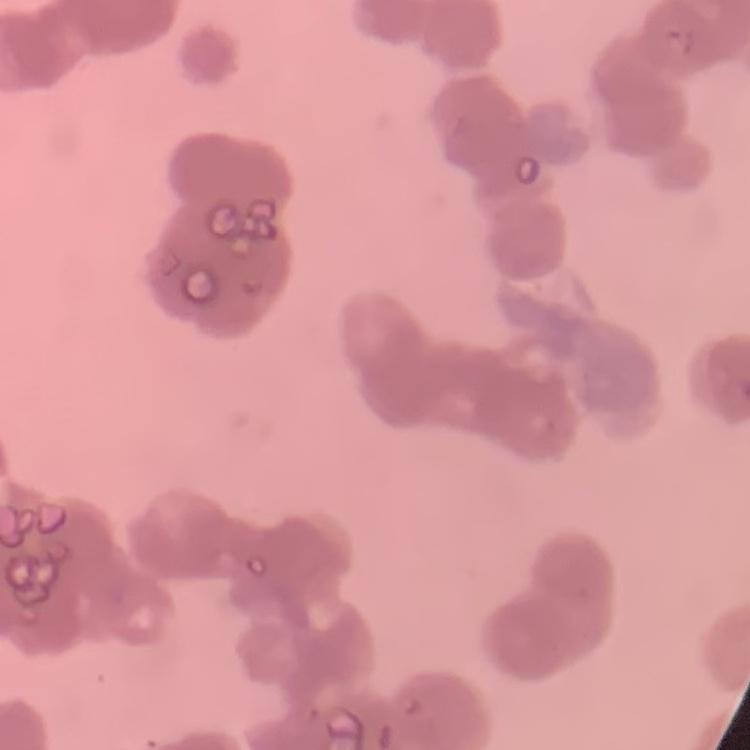

The erythrocytes exhibit rouleaux formation. Thin peripheral smear. Square crop of a larger photomicrograph. Field's or Giemsa stain.